Identify the blood parasite species.
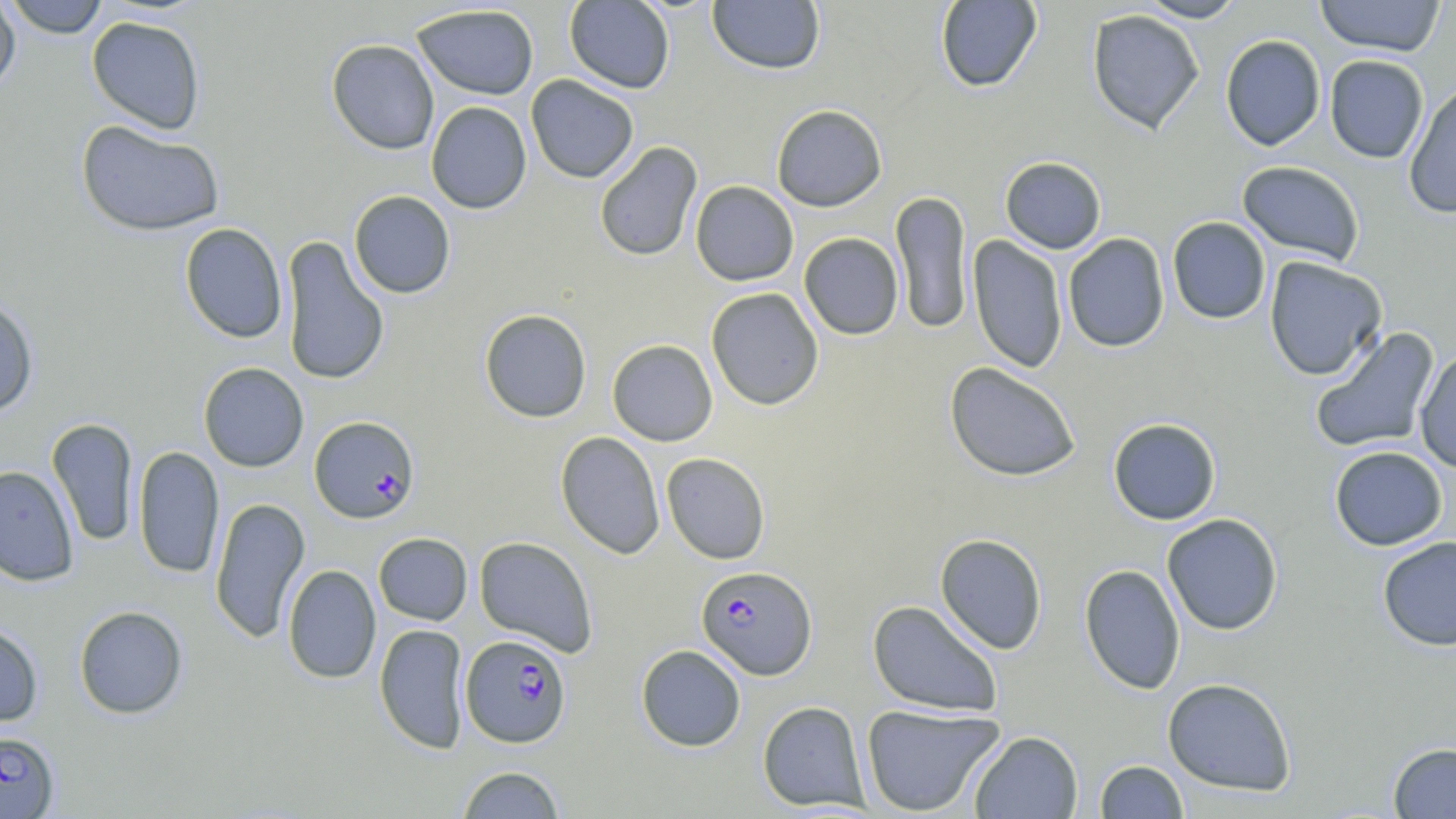

Plasmodium falciparum.

image size = 1456×819 pixels
stain = May-Grünwald-Giemsa
preparation = thin blood film
uninfected red blood cell locations = approximate bounding boxes as (x1, y1, x2, y2) in pixels: (0, 0, 21, 96), (4, 0, 110, 38), (707, 0, 826, 75), (934, 0, 1043, 93), (1136, 0, 1247, 22), (1314, 0, 1446, 57), (564, 1, 675, 93), (412, 4, 539, 100), (1086, 9, 1204, 134), (86, 15, 206, 134), (1089, 19, 1328, 136), (1220, 34, 1326, 151), (326, 39, 439, 155), (1324, 55, 1429, 163), (526, 75, 639, 183), (1403, 79, 1456, 219), (426, 101, 532, 214), (771, 104, 887, 212), (75, 120, 225, 236), (594, 141, 703, 262), (1000, 156, 1106, 254), (1237, 160, 1365, 266), (690, 181, 799, 286), (349, 190, 456, 298), (891, 190, 972, 334), (1167, 217, 1271, 324), (179, 222, 288, 343), (799, 233, 904, 340), (1063, 233, 1170, 352), (281, 235, 390, 386), (968, 235, 1068, 373), (1264, 256, 1388, 381), (705, 287, 824, 410), (0, 296, 39, 417), (479, 309, 592, 423), (1309, 326, 1440, 455), (607, 339, 718, 446), (1414, 349, 1456, 474), (199, 362, 308, 472), (944, 362, 1081, 482), (1108, 417, 1221, 525), (47, 418, 139, 547), (555, 431, 665, 559), (1329, 445, 1448, 551), (133, 446, 224, 579), (661, 452, 770, 565), (0, 465, 79, 586), (210, 497, 310, 643), (1162, 513, 1283, 636), (374, 533, 472, 625), (934, 533, 1048, 654), (474, 536, 599, 657), (1377, 536, 1456, 651), (1079, 563, 1186, 694), (282, 564, 381, 684), (867, 599, 1003, 718), (73, 605, 188, 719), (0, 622, 44, 727), (374, 623, 470, 754), (635, 644, 746, 751), (1162, 677, 1296, 796), (757, 700, 870, 811), (860, 704, 1005, 816), (969, 730, 1083, 818), (1388, 742, 1456, 818), (1094, 760, 1188, 818), (456, 766, 565, 817)
Plasmodium falciparum-infected red blood cell locations = approximate bounding boxes as (x1, y1, x2, y2) in pixels: (310, 416, 420, 523), (696, 565, 817, 680), (461, 634, 572, 748), (0, 730, 59, 818)
field of view = single
magnification = 1000x
modality = light microscopy